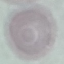
Malaria status: uninfected. Automatically extracted cell patch, resized to 64 × 64 pixels. Acquired by smartphone through the microscope eyepiece. Thin smear of blood. Giemsa stain.